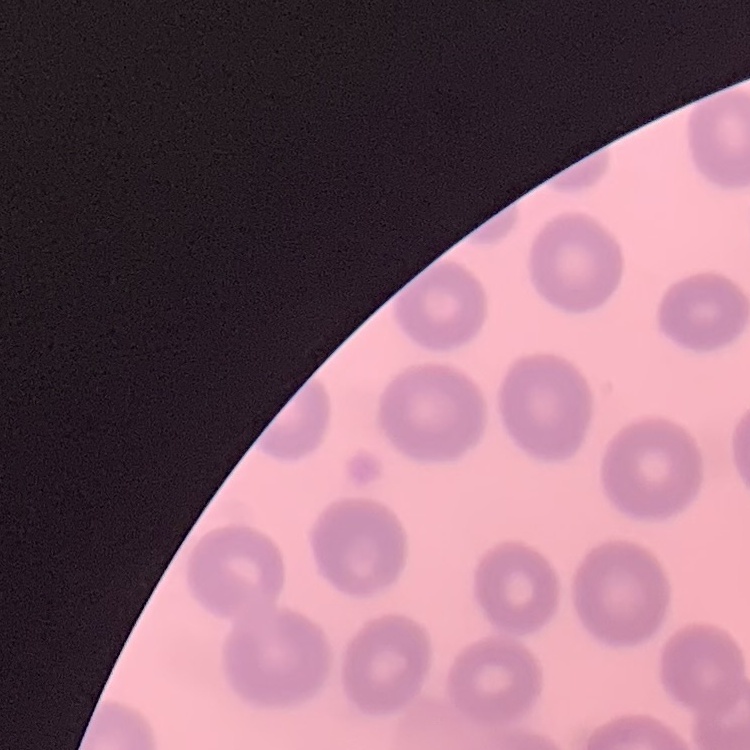
Summary:
  - Red blood cell morphology: no rouleaux formation
  - Image type: square crop of a larger photomicrograph
  - Stain: Field's or Giemsa
  - Preparation: thin blood smear